Give the position of every leukocyte visible.
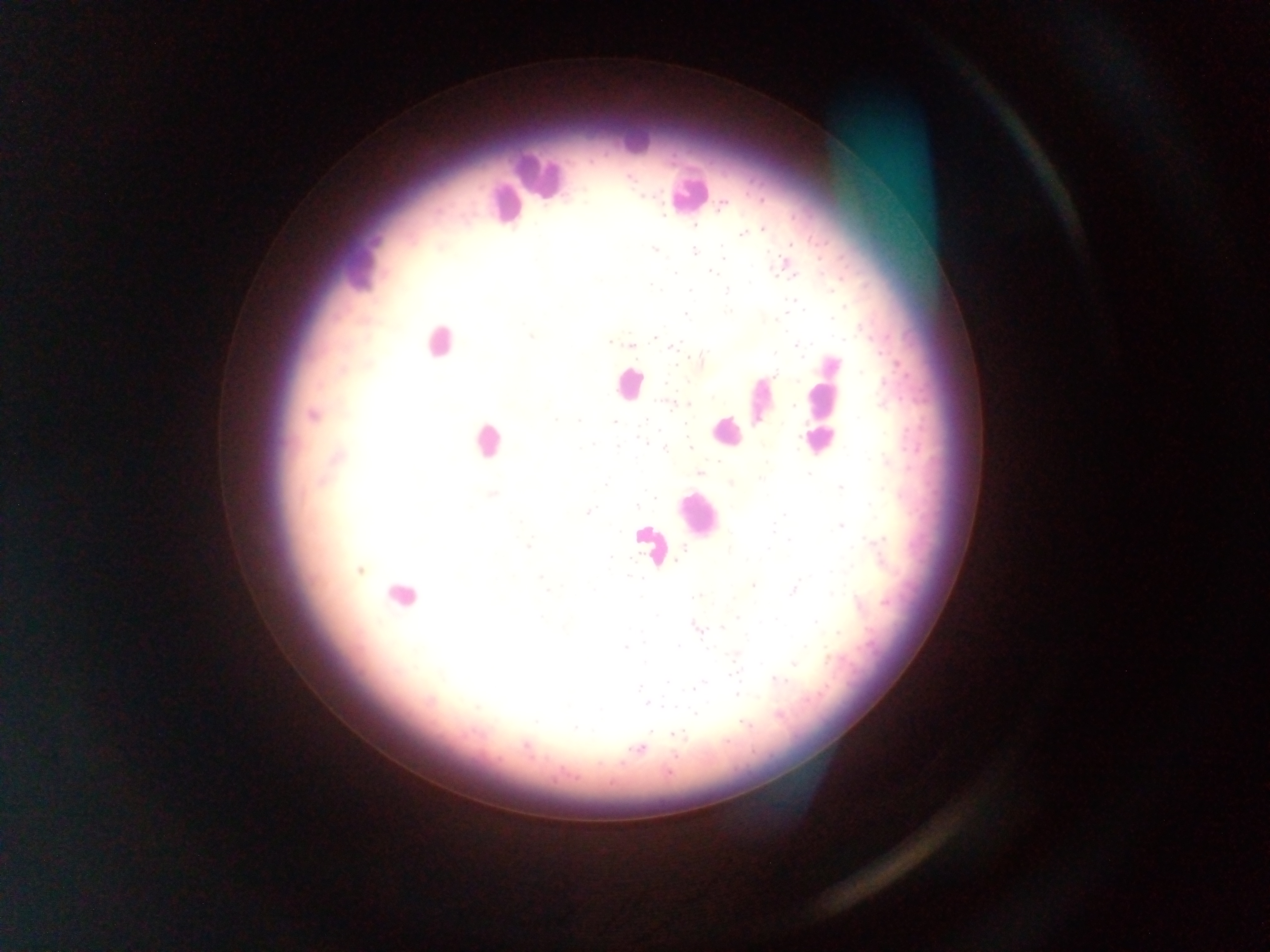
Approximate centers as x y in pixels.
Leukocytes: 635 136; 539 175; 688 194; 504 204; 357 268; 439 342; 628 384; 825 384; 760 401; 726 431; 821 439; 486 440; 696 514; 649 544; 400 596.

{
  "malaria_parasite_locations": "approximate centers as x y in pixels: 628 178; 722 206; 664 217; 762 229; 742 234; 655 250; 693 251; 724 255; 785 267; 710 271; 675 273; 650 286; 727 290; 689 292; 729 311; 685 315; 531 336; 655 337; 610 342; 631 346; 797 346; 674 347; 695 359; 776 374; 664 384; 669 403; 687 404; 795 405; 312 415; 555 419; 578 421; 613 421; 647 422; 642 440; 593 444; 617 446; 690 447; 664 448; 700 472; 809 473; 730 483; 605 484; 841 487; 493 494; 653 497; 637 506; 588 512; 783 515; 841 525; 527 546; 879 549; 611 556; 361 571; 541 577; 753 586; 547 590; 795 590; 696 596; 738 618; 816 621; 697 627; 721 627; 625 648; 793 663; 732 674; 777 680; 697 686; 639 687; 737 695; 649 704; 695 713; 779 715; 744 724; 677 736; 639 748",
  "field_of_view": "single",
  "preparation": "thick blood smear",
  "country": "Ghana",
  "image_size": "1270×952 pixels",
  "capture": "mobile-phone photograph through a microscope"
}